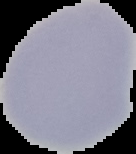
Result: no malaria parasites detected. From a thin blood smear. Image is 136×154 pixels. The area outside the segmented cell region is set to black.